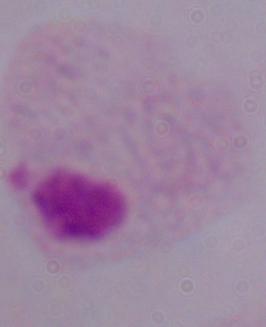

Summary:
  - Modality: micrograph
  - Identification: trichomonad
  - Magnification: 1000x